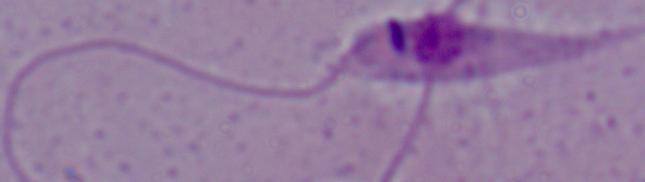
Summary:
  - Identification: Leishmania
  - Magnification: 1000x
  - Modality: photomicrograph